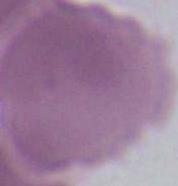

identification = erythrocyte
modality = photomicrograph
magnification = 1000x